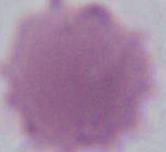
Summary:
  - Magnification: 1000x
  - Modality: photomicrograph
  - Identification: erythrocyte